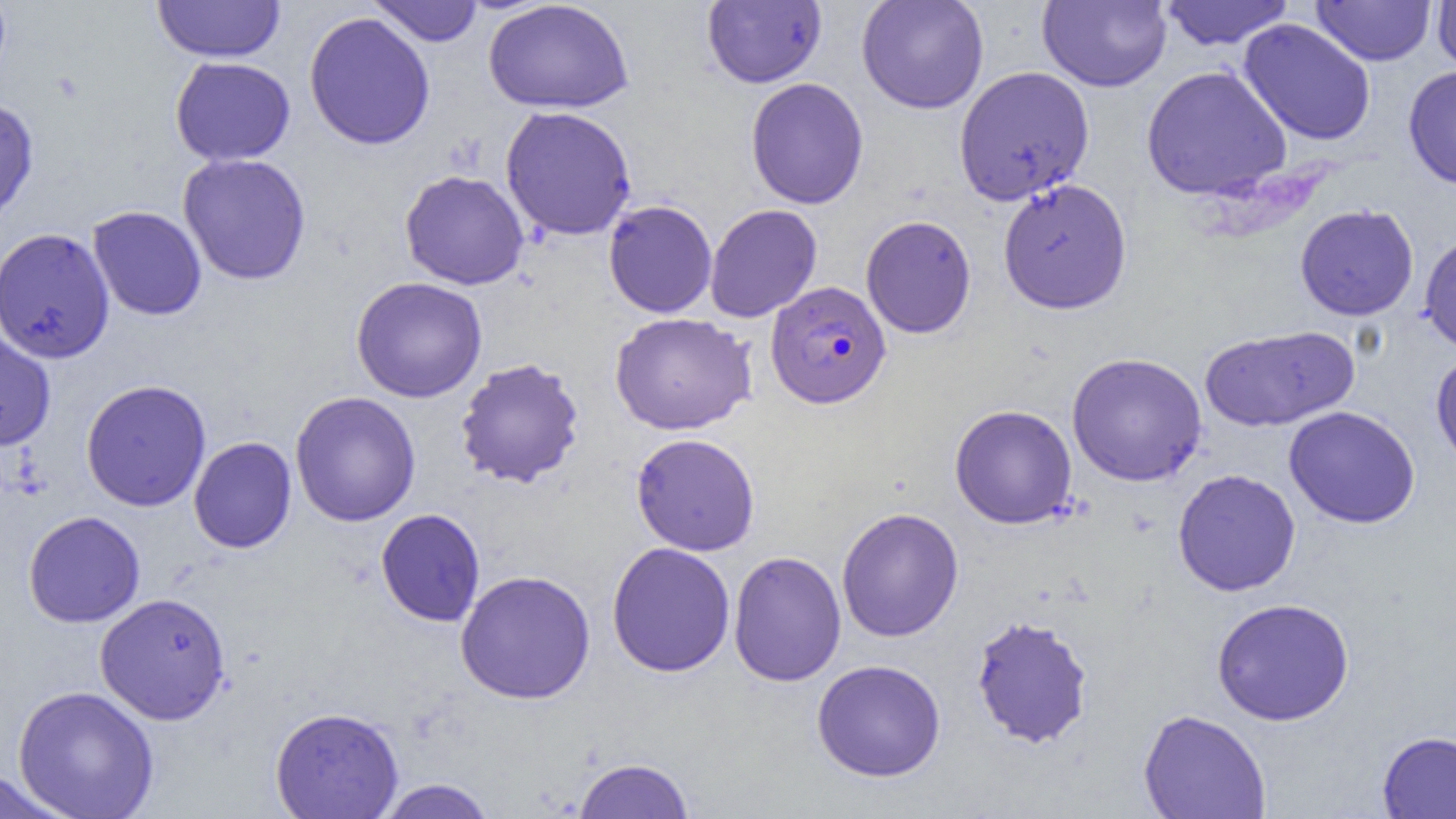

Approximate bounding boxes as named x1/y1/x2/y2 corners in pixels. Uninfected red blood cell locations: (x1=368, y1=0, x2=484, y2=46), (x1=856, y1=0, x2=989, y2=114), (x1=1037, y1=0, x2=1172, y2=92), (x1=1159, y1=0, x2=1294, y2=50), (x1=1311, y1=0, x2=1436, y2=66), (x1=152, y1=1, x2=285, y2=63), (x1=483, y1=1, x2=634, y2=115), (x1=702, y1=1, x2=826, y2=88), (x1=1431, y1=1, x2=1456, y2=76), (x1=303, y1=12, x2=435, y2=150), (x1=1238, y1=18, x2=1377, y2=146), (x1=169, y1=56, x2=296, y2=166), (x1=1140, y1=65, x2=1292, y2=201), (x1=1403, y1=65, x2=1456, y2=190), (x1=953, y1=66, x2=1095, y2=206), (x1=745, y1=77, x2=869, y2=209), (x1=0, y1=98, x2=39, y2=225), (x1=500, y1=105, x2=637, y2=241), (x1=177, y1=153, x2=312, y2=285), (x1=400, y1=170, x2=529, y2=290), (x1=997, y1=178, x2=1133, y2=315), (x1=603, y1=200, x2=717, y2=318), (x1=705, y1=204, x2=823, y2=323), (x1=1294, y1=204, x2=1419, y2=321), (x1=87, y1=206, x2=207, y2=320), (x1=860, y1=215, x2=977, y2=338), (x1=0, y1=227, x2=115, y2=364), (x1=1419, y1=232, x2=1456, y2=354), (x1=351, y1=276, x2=488, y2=403), (x1=610, y1=312, x2=757, y2=435), (x1=1199, y1=325, x2=1359, y2=433), (x1=0, y1=326, x2=56, y2=451), (x1=1431, y1=350, x2=1456, y2=474), (x1=1067, y1=352, x2=1207, y2=486), (x1=454, y1=357, x2=585, y2=489), (x1=81, y1=379, x2=211, y2=513), (x1=290, y1=391, x2=421, y2=526), (x1=949, y1=404, x2=1077, y2=529), (x1=1283, y1=405, x2=1421, y2=528), (x1=631, y1=432, x2=760, y2=556), (x1=188, y1=436, x2=297, y2=553), (x1=1172, y1=468, x2=1301, y2=596), (x1=836, y1=507, x2=964, y2=642), (x1=375, y1=508, x2=485, y2=627), (x1=22, y1=511, x2=146, y2=627), (x1=606, y1=542, x2=735, y2=677), (x1=728, y1=550, x2=846, y2=687), (x1=455, y1=569, x2=596, y2=704), (x1=94, y1=592, x2=231, y2=725), (x1=1211, y1=597, x2=1355, y2=726), (x1=970, y1=614, x2=1094, y2=748), (x1=811, y1=659, x2=946, y2=782), (x1=12, y1=685, x2=160, y2=818), (x1=269, y1=706, x2=404, y2=819), (x1=1138, y1=709, x2=1272, y2=819), (x1=1377, y1=730, x2=1456, y2=819), (x1=573, y1=757, x2=695, y2=818), (x1=0, y1=769, x2=71, y2=819), (x1=375, y1=778, x2=498, y2=818). Plasmodium falciparum-infected red blood cell locations: (x1=765, y1=281, x2=891, y2=409). Slide-level diagnosis: Plasmodium falciparum. Optical microscopy. Thin blood film. Image is 1456×819 pixels. Captured at 1000x magnification. One field of a larger specimen.